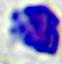
Summary:
  - Modality: photomicrograph
  - Identification: white blood cell
  - Magnification: 400x